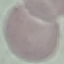

malaria status = uninfected
image type = cell patch, automatically extracted from a larger field of view and resized to 64 × 64 pixels
stain = Giemsa
capture = smartphone camera at the microscope eyepiece
preparation = thin blood smear